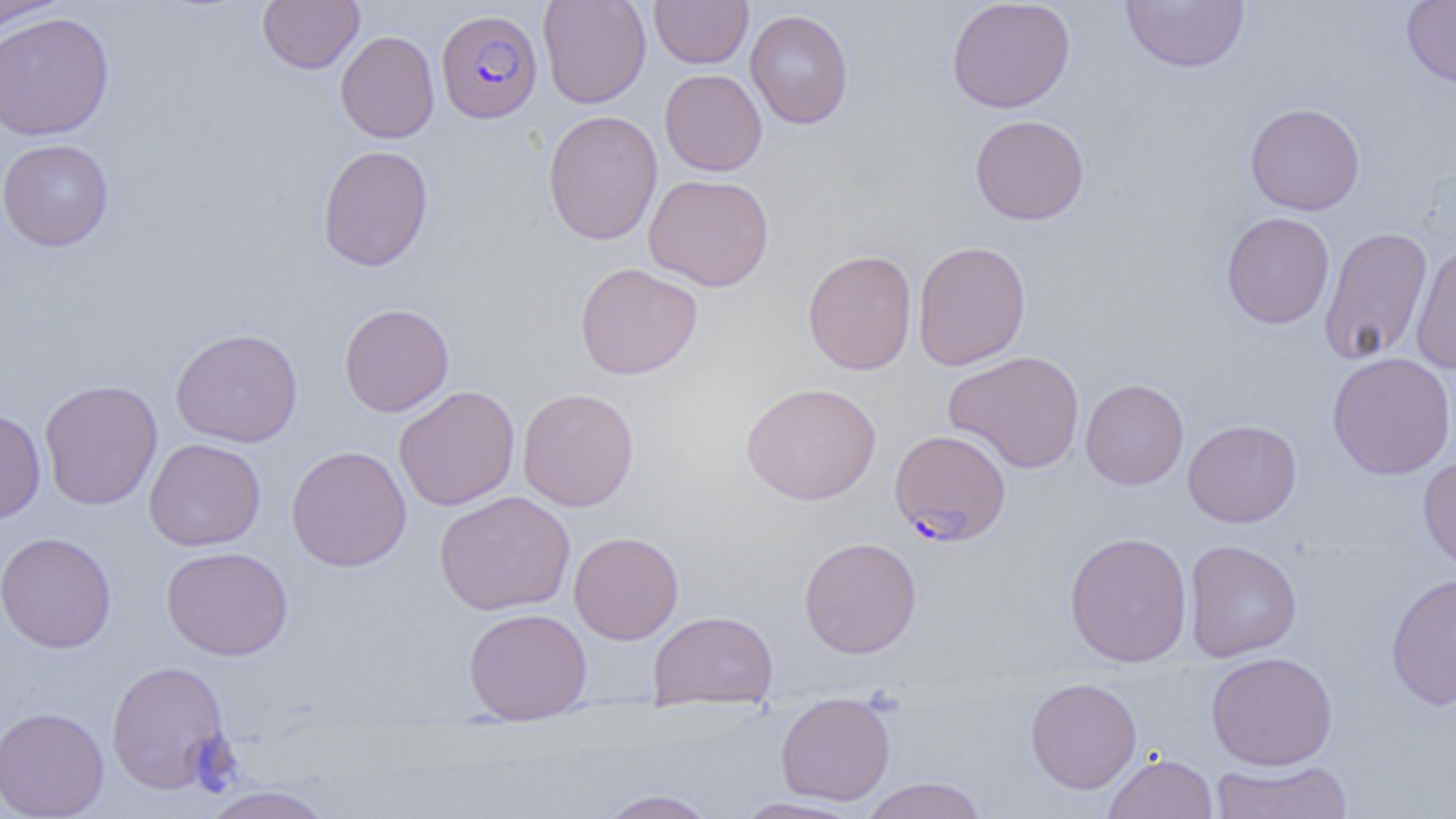
Summary:
  - Coordinate format: approximate bounding boxes as (x1, y1, x2, y2) in pixels
  - Uninfected red blood cell locations: (0, 0, 69, 33), (257, 0, 364, 74), (538, 0, 652, 108), (649, 0, 753, 68), (946, 0, 1076, 113), (1121, 0, 1250, 73), (1401, 0, 1456, 87), (745, 9, 854, 129), (0, 12, 114, 141), (335, 30, 439, 143), (659, 69, 767, 176), (1245, 103, 1366, 215), (542, 110, 663, 245), (969, 114, 1090, 225), (0, 138, 114, 252), (317, 144, 434, 272), (643, 173, 774, 292), (1221, 212, 1334, 329), (1318, 225, 1433, 365), (912, 240, 1032, 370), (1411, 241, 1456, 374), (802, 248, 917, 376), (574, 262, 703, 380), (339, 303, 454, 417), (170, 327, 303, 448), (943, 350, 1085, 474), (1326, 352, 1456, 479), (1080, 378, 1189, 490), (39, 379, 162, 510), (740, 382, 881, 506), (393, 385, 520, 511), (517, 387, 640, 511), (0, 407, 46, 524), (1182, 419, 1302, 527), (144, 438, 266, 551), (286, 445, 412, 572), (1418, 457, 1456, 575), (434, 491, 575, 615), (569, 531, 684, 645), (1064, 531, 1193, 668), (0, 532, 116, 653), (799, 536, 922, 659), (1184, 539, 1302, 662), (160, 545, 293, 661), (1385, 571, 1456, 711), (464, 607, 592, 724), (649, 610, 778, 710), (1205, 651, 1338, 770), (106, 659, 232, 794), (1025, 677, 1142, 794), (776, 692, 895, 806), (0, 705, 109, 819), (1104, 752, 1217, 819), (1208, 759, 1355, 818), (860, 776, 987, 819), (197, 785, 338, 819), (596, 789, 718, 818), (730, 796, 869, 818)
  - Plasmodium falciparum-infected red blood cell locations: (436, 9, 542, 123), (889, 429, 1011, 546)
  - Slide-level diagnosis: Plasmodium falciparum
  - Modality: optical microscopy
  - Preparation: thin blood smear
  - Field of view: single
  - Image size: 1456×819 pixels
  - Magnification: 1000x